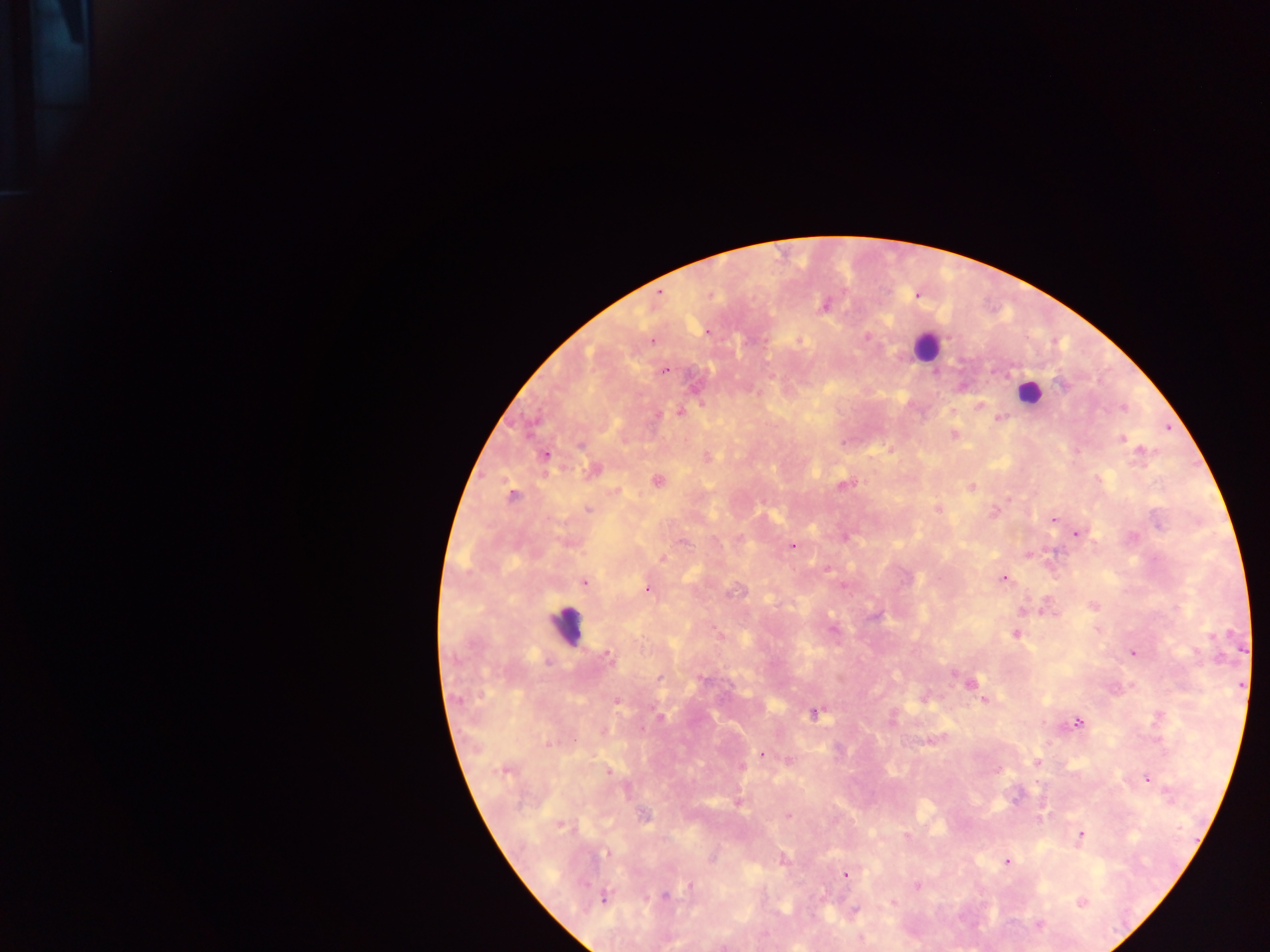
Approximate centers as {x, y} in pixels.
Summary:
  - Malaria parasite locations: {658, 294}, {916, 295}, {824, 304}, {707, 332}, {867, 337}, {652, 341}, {664, 370}, {979, 405}, {1121, 406}, {951, 410}, {680, 412}, {999, 418}, {953, 434}, {1120, 437}, {1141, 452}, {544, 456}, {707, 456}, {592, 470}, {657, 480}, {842, 484}, {970, 486}, {512, 497}, {588, 509}, {938, 509}, {993, 513}, {1052, 518}, {1075, 532}, {844, 536}, {792, 546}, {1027, 553}, {662, 558}, {827, 567}, {1003, 578}, {583, 582}, {843, 584}, {647, 588}, {1093, 605}, {1022, 610}, {833, 628}, {1016, 633}, {1132, 653}, {607, 655}, {660, 678}, {968, 683}, {1241, 685}, {924, 698}, {616, 700}, {984, 700}, {814, 713}, {1157, 718}, {1077, 722}, {931, 739}, {761, 755}, {789, 760}, {1036, 762}, {741, 767}, {505, 769}, {997, 770}, {608, 771}, {1146, 778}, {737, 802}, {644, 816}, {788, 816}, {560, 824}, {1080, 835}, {906, 836}, {1006, 861}, {845, 875}, {916, 885}, {690, 887}, {665, 895}, {603, 897}, {892, 902}, {1080, 902}, {854, 910}, {1038, 924}
  - Leukocyte locations: {925, 346}, {1029, 392}, {565, 626}
  - Capture: mobile-phone photograph through a microscope
  - Field of view: single
  - Preparation: thick blood smear
  - Image size: 1270×952 pixels
  - Country: Ghana